Classify this cell by malaria status.
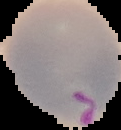
It is parasitized.

Image is 121×130 pixels. Segmented cell region on a black background. From a thin blood film.